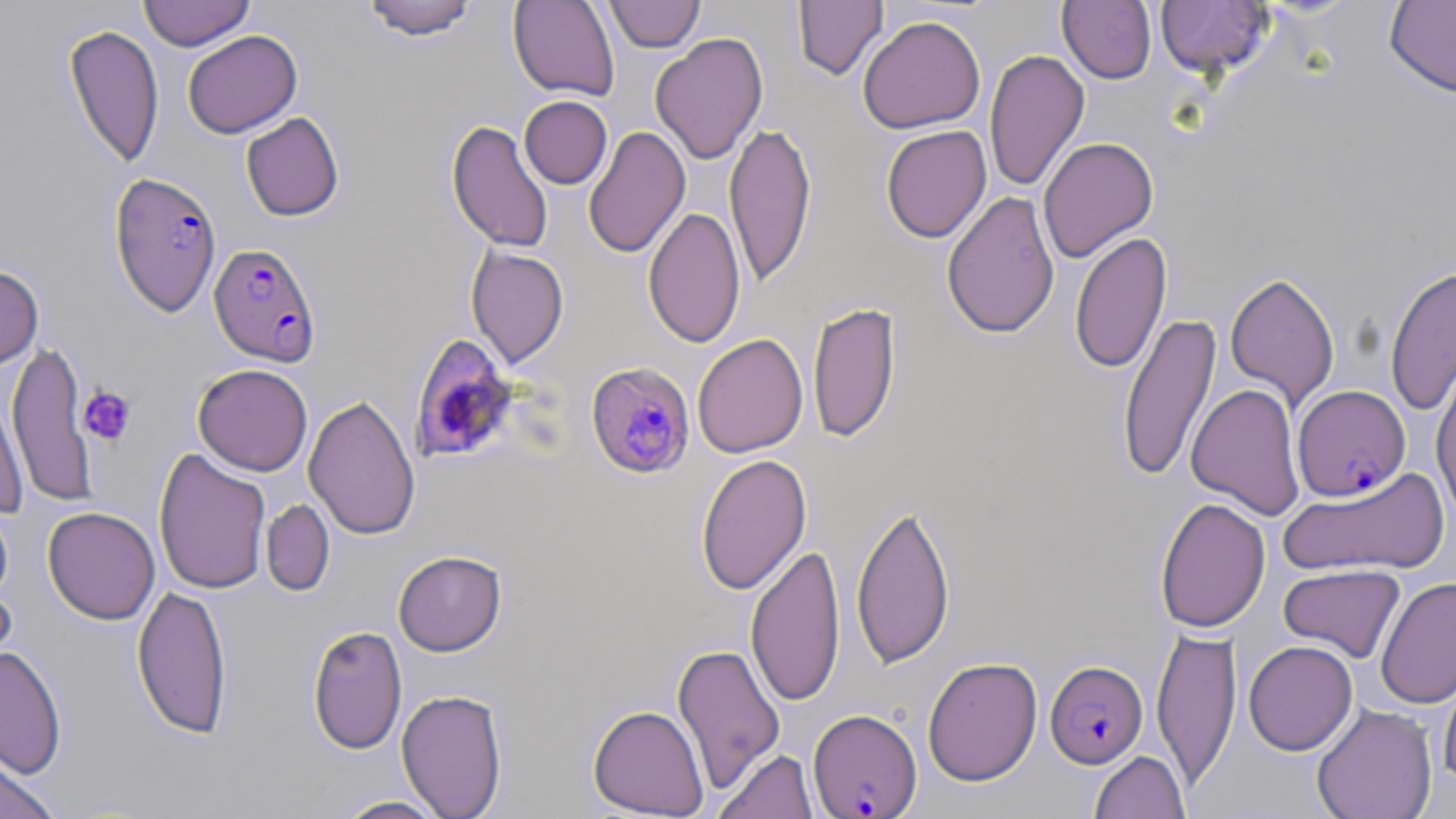
Summary:
  - Coordinate format: approximate bounding boxes as (x1, y1, x2, y2) in pixels
  - Platelet locations: (78, 385, 136, 445)
  - Uninfected red blood cell locations: (138, 0, 255, 51), (361, 0, 480, 41), (508, 0, 620, 101), (793, 0, 889, 82), (1058, 0, 1157, 84), (1155, 0, 1274, 79), (604, 1, 706, 52), (1384, 1, 1456, 99), (857, 15, 986, 134), (63, 24, 164, 169), (182, 30, 302, 139), (650, 32, 768, 165), (984, 48, 1090, 194), (519, 95, 612, 189), (241, 112, 344, 221), (447, 120, 554, 253), (724, 120, 816, 288), (880, 125, 992, 243), (583, 126, 690, 260), (1038, 137, 1159, 263), (942, 191, 1060, 339), (643, 205, 747, 349), (1070, 231, 1171, 374), (466, 245, 569, 368), (0, 264, 44, 369), (1385, 265, 1456, 416), (1225, 271, 1340, 409), (807, 300, 901, 443), (1117, 311, 1221, 482), (692, 333, 808, 458), (6, 339, 96, 509), (193, 364, 313, 476), (1431, 367, 1456, 523), (1187, 383, 1305, 520), (1, 385, 30, 518), (303, 393, 420, 540), (153, 447, 271, 595), (696, 452, 812, 596), (1279, 467, 1449, 578), (1154, 497, 1270, 633), (0, 498, 14, 607), (261, 499, 335, 597), (851, 501, 955, 670), (42, 506, 160, 625), (746, 541, 845, 708), (393, 550, 507, 656), (1277, 564, 1405, 663), (1376, 577, 1456, 709), (0, 581, 18, 684), (132, 584, 232, 740), (307, 625, 407, 754), (1151, 625, 1242, 790), (1243, 640, 1358, 755), (672, 641, 786, 794), (0, 645, 67, 779), (922, 657, 1042, 786), (1438, 662, 1456, 789), (396, 688, 508, 819), (1312, 703, 1437, 819), (588, 704, 709, 817), (713, 747, 819, 819), (1089, 750, 1190, 818), (0, 751, 62, 819), (330, 795, 451, 818)
  - Plasmodium falciparum-infected red blood cell locations: (109, 171, 223, 317), (209, 242, 322, 367), (410, 332, 519, 465), (586, 362, 696, 479), (1292, 384, 1410, 501), (1045, 660, 1148, 768), (807, 708, 922, 818)
  - Slide-level diagnosis: Plasmodium falciparum
  - Magnification: 1000x
  - Field of view: single
  - Preparation: thin blood film
  - Image size: 1456×819 pixels
  - Modality: light microscopy
  - Stain: May-Grünwald-Giemsa